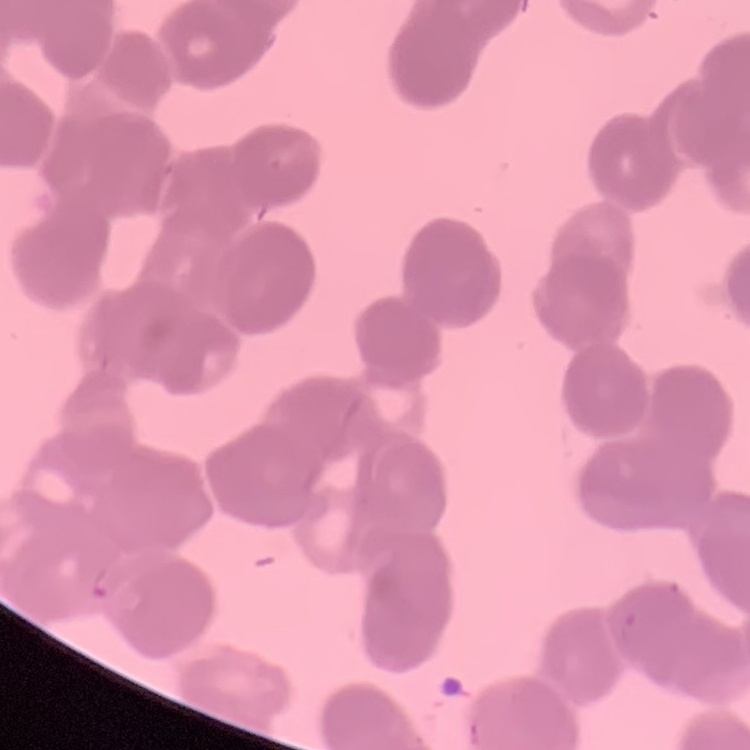 The red blood cells exhibit rouleaux formation. Thin peripheral smear. One tile cut from a larger photomicrograph. Field's or Giemsa stain.